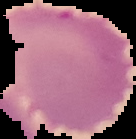
{
  "preparation": "thin blood smear",
  "image_size": "136×139 pixels",
  "image_type": "cell region segmented out of the field of view; surrounding area masked to black",
  "result": "negative for Plasmodium parasites"
}